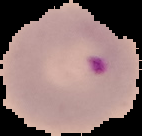
image type = segmented cell region on a black background
malaria status = parasitized
preparation = thin blood smear
image size = 142×136 pixels